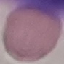
Summary:
  - Result: no malaria parasites seen
  - Image type: cell patch, automatically extracted from a larger field of view and resized to 64 × 64 pixels
  - Stain: Giemsa
  - Preparation: thin blood smear
  - Capture: smartphone through the microscope eyepiece